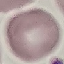 Result: negative for malaria parasites. Giemsa stain. Cell patch, automatically extracted from a larger field of view and resized to 64 × 64 pixels. Thin blood smear. Photographed with a smartphone camera at the microscope eyepiece.